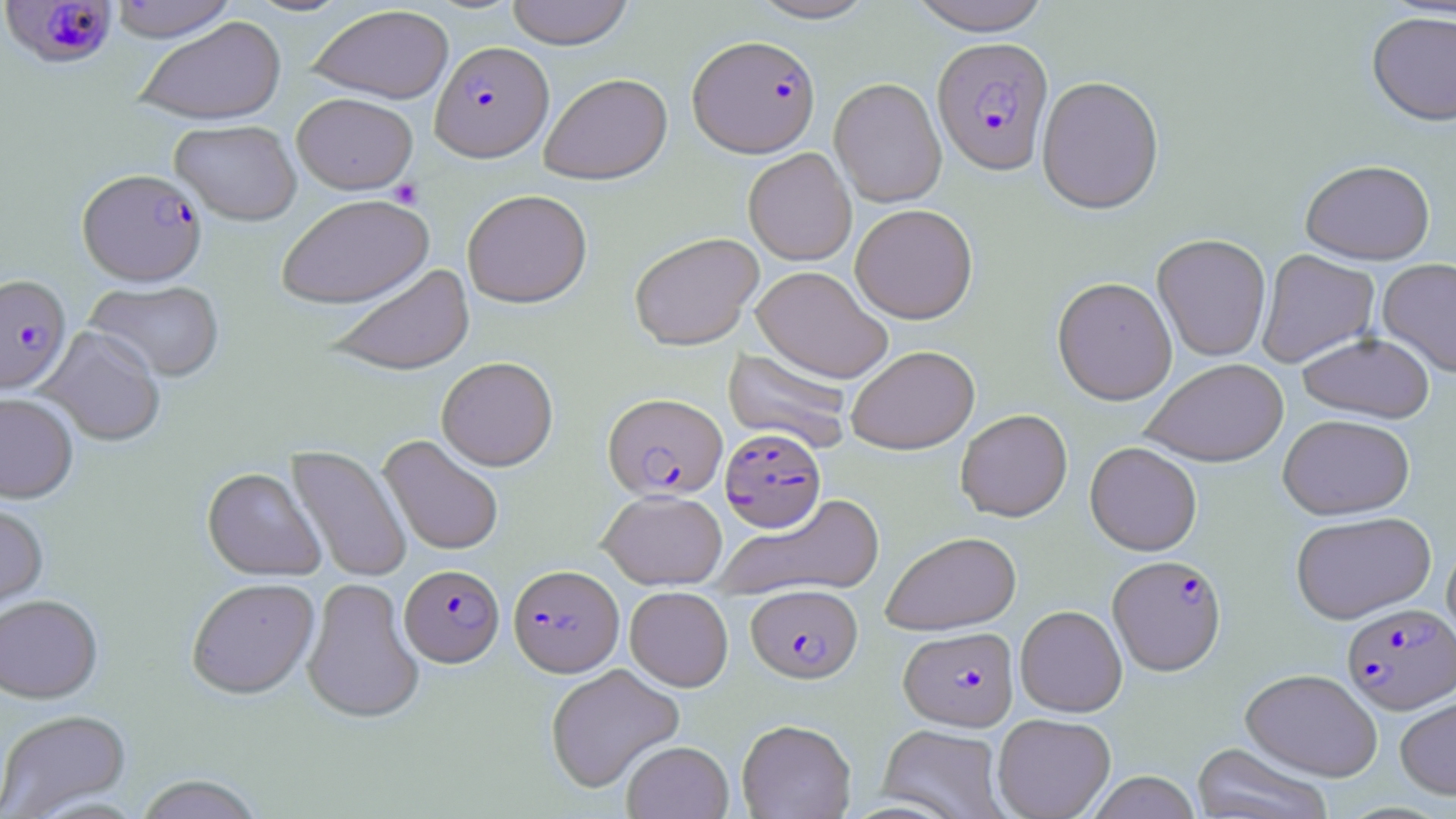
Approximate bounding boxes as (x1,y1)-(x2,y2) corner pairs in pixels. Platelet locations: (389,180)-(423,209). Plasmodium falciparum-infected red blood cell locations: (1,0)-(119,71), (688,34)-(821,157), (932,37)-(1053,175), (430,40)-(553,161), (78,169)-(206,284), (0,273)-(71,394), (603,392)-(727,500), (720,427)-(826,532), (1108,554)-(1227,675), (399,564)-(504,667), (508,564)-(623,676), (746,583)-(863,684), (1342,603)-(1455,713), (899,625)-(1019,731). Uninfected red blood cell locations: (108,0)-(239,42), (505,0)-(635,49), (745,0)-(880,23), (903,0)-(1055,34), (307,4)-(453,104), (1367,10)-(1456,126), (134,16)-(287,125), (539,72)-(672,184), (1036,75)-(1164,215), (829,77)-(947,207), (291,92)-(418,194), (170,119)-(302,225), (743,148)-(857,265), (1300,159)-(1435,264), (462,189)-(593,308), (276,194)-(434,309), (850,203)-(977,323), (628,232)-(763,350), (1152,234)-(1271,362), (1256,249)-(1380,368), (1377,258)-(1456,378), (324,264)-(475,375), (751,265)-(892,384), (1052,276)-(1177,405), (84,279)-(226,382), (38,326)-(166,446), (1297,332)-(1435,423), (846,345)-(979,454), (723,347)-(853,452), (436,356)-(558,471), (1141,358)-(1288,467), (0,391)-(79,503), (955,409)-(1072,522), (1278,414)-(1415,520), (379,435)-(504,555), (1085,441)-(1202,555), (287,445)-(412,583), (202,467)-(324,580), (598,489)-(727,589), (714,493)-(885,601), (0,499)-(49,619), (1291,511)-(1437,623), (881,531)-(1021,635), (1441,540)-(1456,655), (186,577)-(320,699), (302,577)-(424,724), (625,586)-(733,691), (0,594)-(104,703), (1015,605)-(1127,717), (545,663)-(685,793), (1240,668)-(1382,781), (1395,695)-(1456,799), (0,709)-(132,819), (992,713)-(1116,819), (736,719)-(856,819), (878,724)-(1008,819), (622,740)-(734,819), (1191,742)-(1334,819), (1087,771)-(1201,818), (132,774)-(266,819). Slide-level diagnosis: Plasmodium falciparum. Single field of view. May-Grünwald-Giemsa stain. Image is 1456×819 pixels. Thin blood smear. Optical microscopy. Captured at 1000x magnification.